Report the malaria status of this cell.
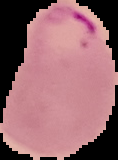
It is parasitized.

Summary:
  - Preparation: thin blood smear
  - Image type: segmented cell region with the area outside set to black
  - Image size: 118×160 pixels